Assess this cell for malaria.
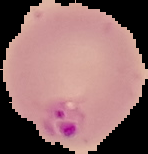

It is parasitized.

preparation: thin blood smear
image_size: 148×154 pixels
image_type: segmented cell region on a black background